Locate every uninfected red blood cell.
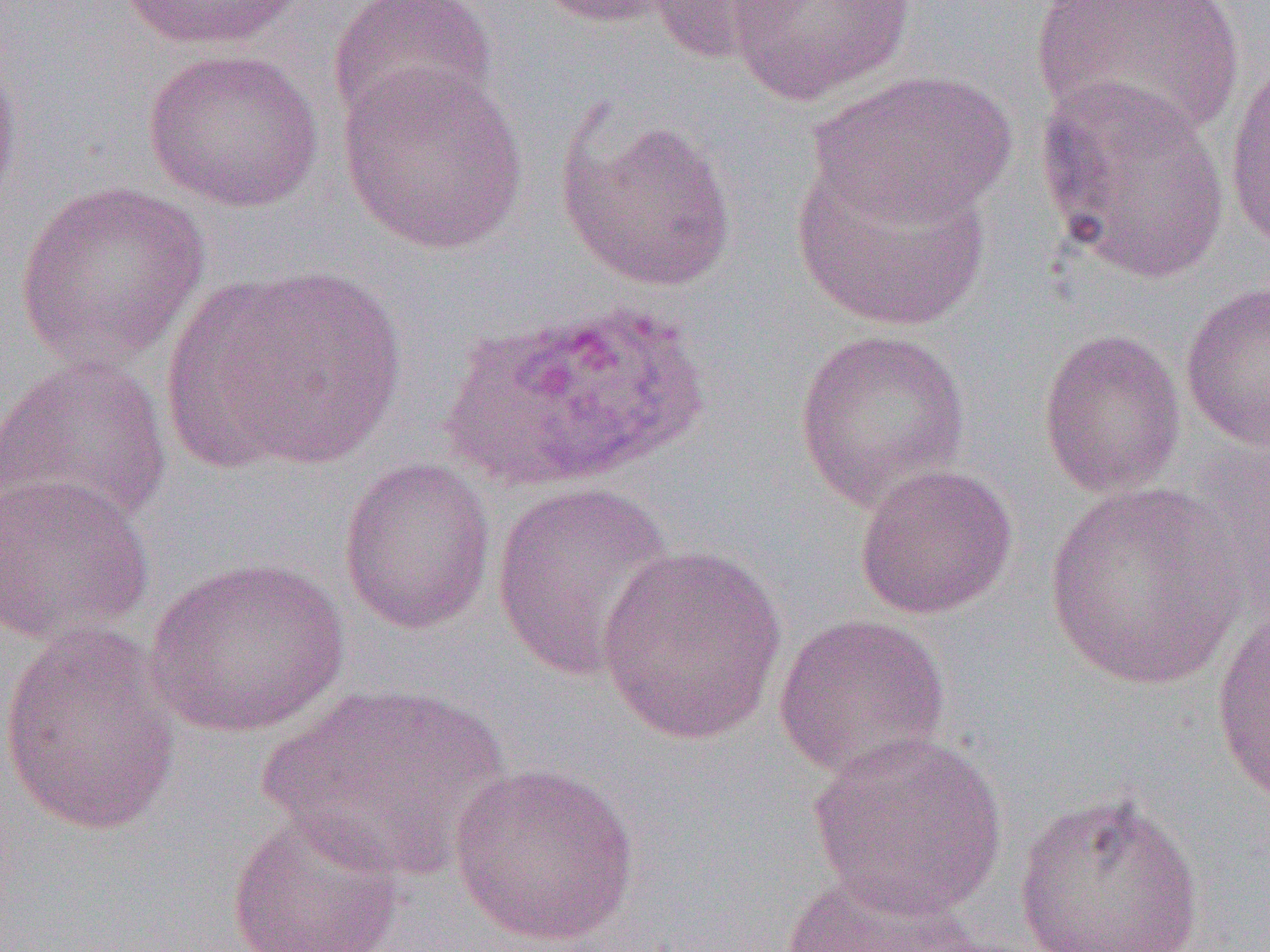

Approximate bounding boxes as [x1, y1, x2, y2] in pixels.
Uninfected red blood cells: [116, 0, 308, 52], [328, 0, 499, 134], [536, 0, 685, 29], [646, 0, 806, 66], [726, 0, 916, 106], [1030, 0, 1245, 145], [0, 43, 23, 220], [142, 46, 325, 214], [1223, 46, 1270, 256], [338, 62, 529, 255], [809, 69, 1018, 229], [1034, 76, 1235, 286], [556, 111, 738, 292], [792, 152, 994, 333], [14, 180, 211, 371], [170, 263, 408, 474], [1179, 280, 1270, 453], [439, 300, 709, 490], [793, 328, 971, 511], [1037, 328, 1187, 500], [0, 354, 172, 531], [337, 457, 497, 635], [853, 464, 1018, 620], [0, 472, 156, 645], [490, 481, 677, 682], [1043, 481, 1248, 692], [596, 545, 787, 744], [146, 556, 351, 739], [1211, 605, 1269, 813], [772, 610, 951, 783], [0, 622, 182, 838], [253, 684, 514, 884], [806, 731, 1009, 919], [447, 761, 640, 948], [1011, 789, 1207, 952], [225, 810, 409, 952], [778, 866, 994, 951].

Slide-level diagnosis: Plasmodium ovale. 1000x magnification. Thin blood film. Light microscopy. One field of a larger specimen. Image is 1270×952 pixels.